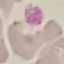
Result: no malaria parasites seen. Photographed with a smartphone camera at the microscope eyepiece. Thin blood film. Giemsa stain. Automatically extracted cell patch, resized to 64 × 64 pixels.